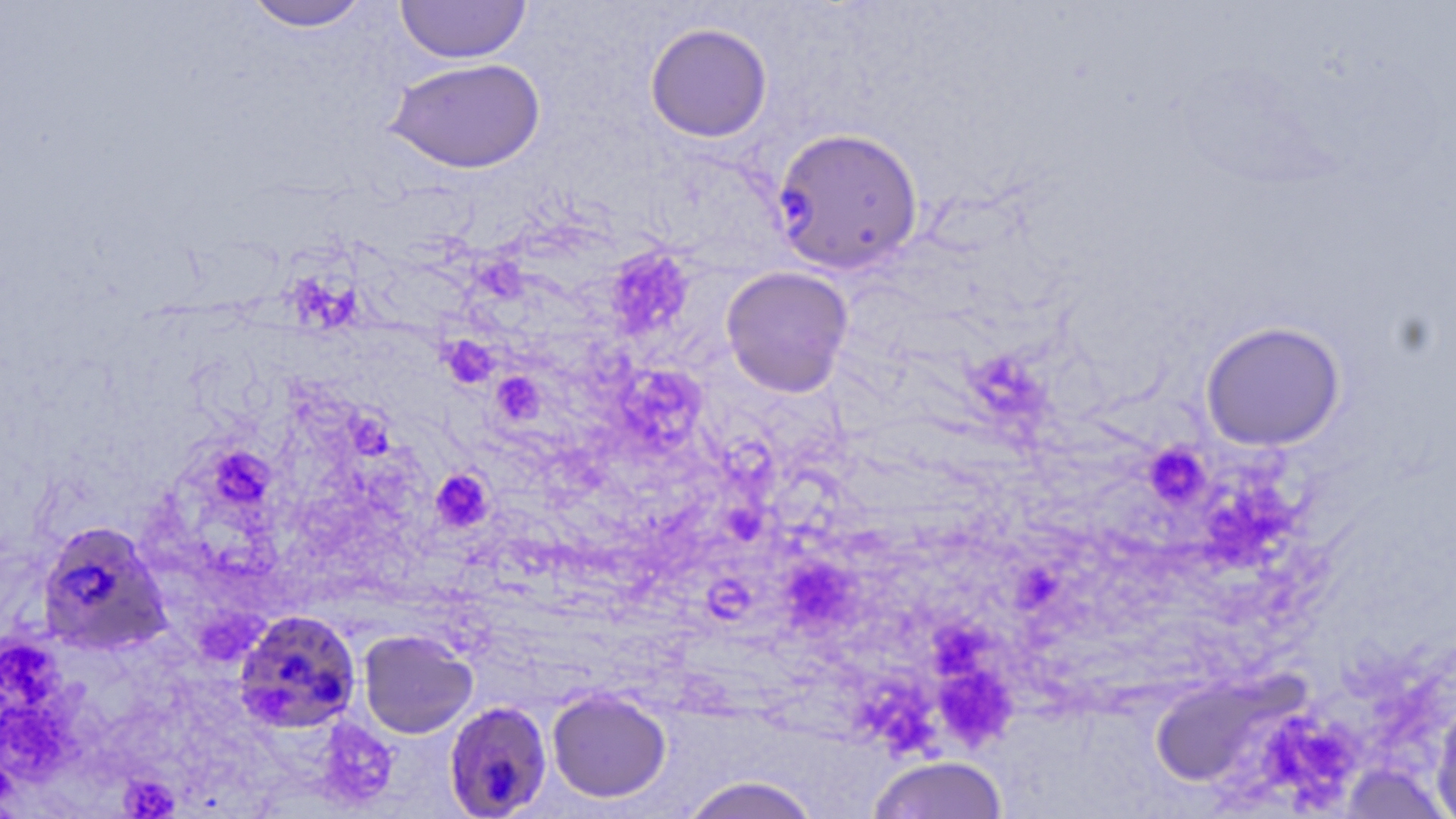

{
  "slide_level_diagnosis": "Plasmodium falciparum",
  "image_size": "1456×819 pixels",
  "preparation": "thin blood smear",
  "uninfected_red_blood_cell_locations": "approximate bounding boxes as [x1, y1, x2, y2] in pixels: [395, 0, 532, 64], [243, 1, 372, 32], [644, 22, 773, 142], [384, 57, 546, 174], [720, 267, 854, 397], [1199, 320, 1346, 451], [358, 629, 479, 739], [1153, 664, 1311, 789], [546, 688, 672, 804], [1431, 693, 1456, 819], [864, 755, 1012, 819], [675, 774, 826, 819]",
  "platelet_locations": "approximate bounding boxes as [x1, y1, x2, y2] in pixels: [611, 251, 692, 329], [480, 257, 527, 298], [290, 277, 363, 322], [441, 336, 501, 389], [968, 357, 1052, 423], [621, 361, 698, 451], [491, 373, 543, 424], [350, 415, 401, 463], [1143, 442, 1210, 509], [214, 452, 268, 495], [430, 468, 493, 532], [1216, 481, 1295, 560], [732, 505, 765, 541], [795, 564, 853, 627], [1015, 569, 1059, 613], [701, 573, 744, 621], [934, 627, 1000, 683], [0, 641, 70, 707], [946, 679, 1018, 751], [857, 683, 940, 759], [4, 700, 83, 773], [315, 719, 399, 810], [1268, 733, 1349, 797], [120, 774, 180, 817]",
  "plasmodium_falciparum_infected_red_blood_cell_locations": "approximate bounding boxes as [x1, y1, x2, y2] in pixels: [772, 127, 925, 275], [36, 520, 172, 657], [229, 609, 361, 733], [443, 700, 554, 818]",
  "field_of_view": "single",
  "modality": "light microscopy",
  "stain": "May-Grünwald-Giemsa",
  "magnification": "1000x"
}